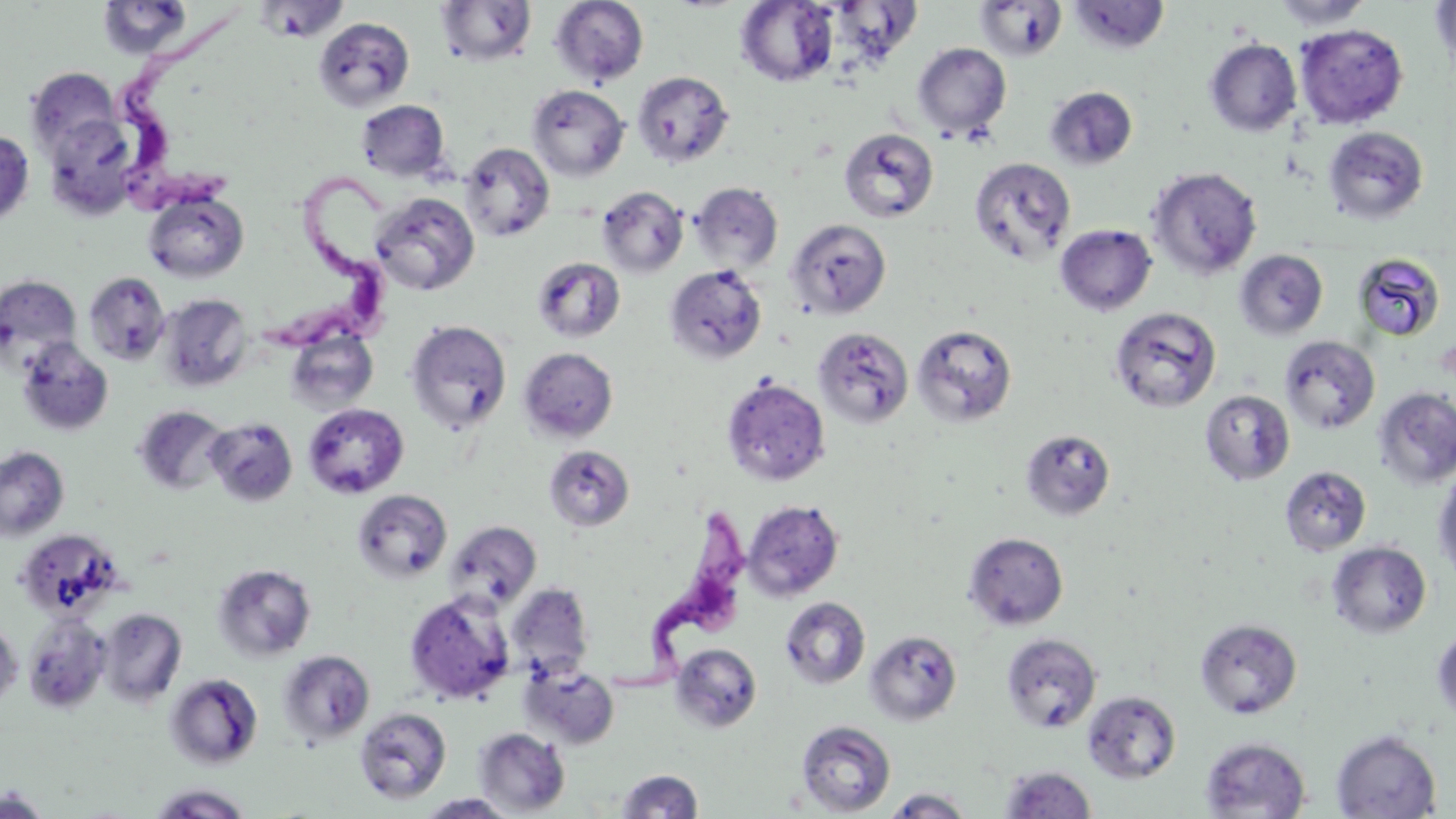

Summary:
  - Coordinate format: approximate bounding boxes as [x1, y1, x2, y2] in pixels
  - Trypanosoma brucei locations: [118, 9, 251, 208], [255, 167, 405, 347], [589, 507, 747, 700]
  - Uninfected red blood cell locations: [106, 0, 194, 57], [257, 0, 348, 42], [550, 0, 648, 86], [974, 0, 1067, 61], [1271, 0, 1372, 31], [1431, 0, 1456, 83], [436, 1, 536, 67], [736, 1, 839, 87], [1068, 1, 1170, 54], [314, 17, 415, 111], [1294, 23, 1409, 129], [1204, 39, 1301, 137], [912, 43, 1011, 139], [26, 68, 122, 162], [632, 70, 734, 168], [528, 84, 629, 181], [1045, 86, 1137, 170], [357, 100, 450, 182], [42, 113, 144, 222], [1323, 126, 1429, 224], [839, 128, 939, 223], [0, 129, 34, 226], [459, 143, 555, 242], [969, 157, 1076, 265], [1147, 166, 1263, 280], [690, 182, 783, 272], [596, 185, 688, 278], [144, 191, 248, 283], [371, 192, 480, 297], [786, 218, 892, 319], [1055, 224, 1157, 316], [1235, 249, 1328, 340], [1353, 253, 1446, 341], [532, 257, 625, 343], [664, 263, 768, 366], [83, 272, 171, 365], [0, 275, 82, 373], [157, 294, 253, 391], [1109, 306, 1221, 413], [405, 320, 512, 434], [912, 323, 1018, 427], [812, 326, 914, 429], [286, 329, 378, 414], [1280, 336, 1380, 434], [17, 338, 114, 437], [519, 347, 619, 442], [721, 376, 830, 487], [1373, 387, 1456, 490], [1199, 390, 1295, 486], [303, 403, 409, 499], [133, 405, 230, 496], [204, 417, 299, 507], [1020, 428, 1116, 522], [543, 444, 635, 532], [0, 446, 69, 542], [1433, 463, 1456, 581], [1280, 465, 1372, 556], [353, 489, 452, 583], [743, 499, 844, 601], [445, 521, 541, 610], [16, 529, 124, 621], [964, 531, 1068, 630], [1327, 541, 1432, 638], [213, 563, 317, 663], [507, 583, 594, 681], [405, 592, 515, 705], [780, 596, 871, 690], [98, 607, 187, 706], [23, 614, 110, 713], [0, 617, 23, 711], [1194, 618, 1303, 719], [1431, 624, 1456, 728], [865, 630, 962, 726], [1001, 633, 1102, 732], [671, 642, 762, 733], [278, 650, 375, 746], [521, 662, 620, 748], [165, 673, 263, 769], [1083, 690, 1181, 783], [354, 707, 451, 804], [796, 720, 896, 816], [474, 727, 570, 815], [1331, 729, 1441, 818], [1200, 737, 1311, 818], [1000, 766, 1096, 818], [616, 769, 703, 818], [147, 784, 253, 818], [1, 787, 52, 818], [882, 787, 975, 818], [416, 793, 519, 818]
  - Slide-level diagnosis: Trypanosoma brucei
  - Field of view: one of a larger specimen
  - Modality: optical microscopy
  - Preparation: thin blood film
  - Image size: 1456×819 pixels
  - Magnification: 1000x
  - Stain: May-Grünwald-Giemsa